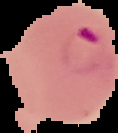

image size = 118×133 pixels
preparation = thin blood smear
malaria status = parasitized
image type = segmented cell region on a black background